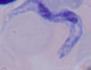
1000x magnification. Photomicrograph. A trypanosome is shown.